Assess the morphology of the red blood cells.
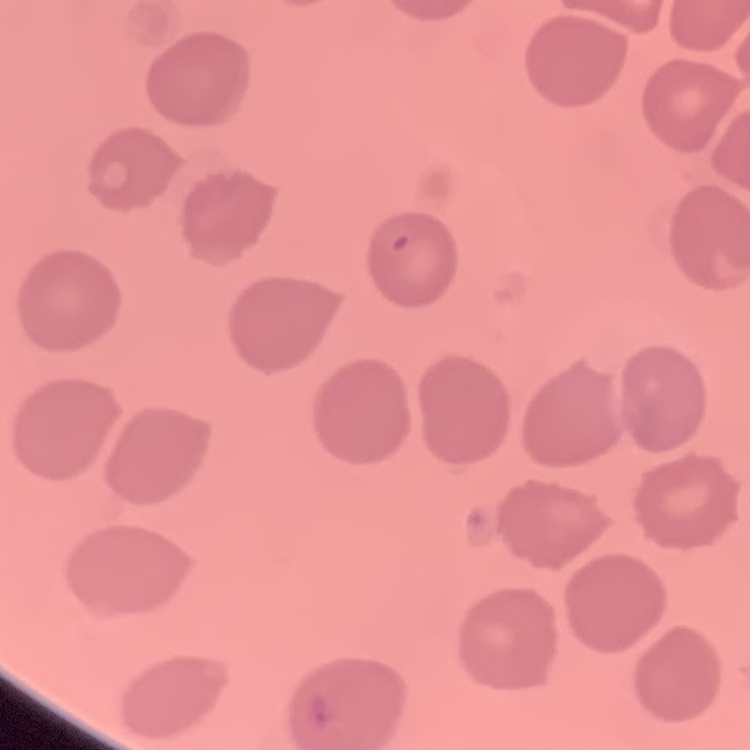
No rouleaux formation.

{
  "stain": "Field's or Giemsa",
  "preparation": "thin blood film",
  "image_type": "one tile cut from a larger photomicrograph"
}